Comment on the morphology of the erythrocytes.
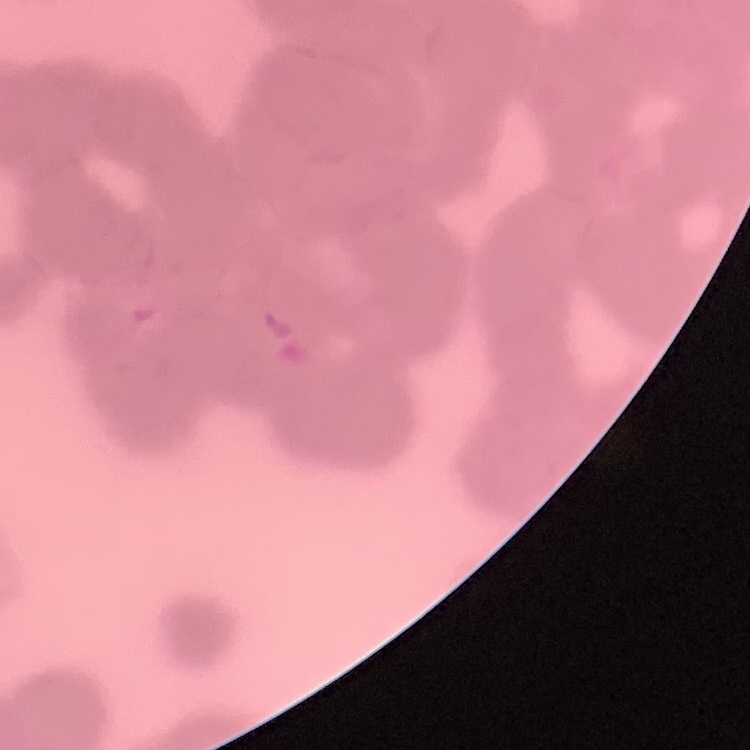

Rouleaux formation.

Stained with either Field's or Giemsa. One tile cut from a larger photomicrograph. Thin blood smear.